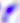
{
  "modality": "photomicrograph",
  "identification": "Toxoplasma gondii",
  "magnification": "400x"
}